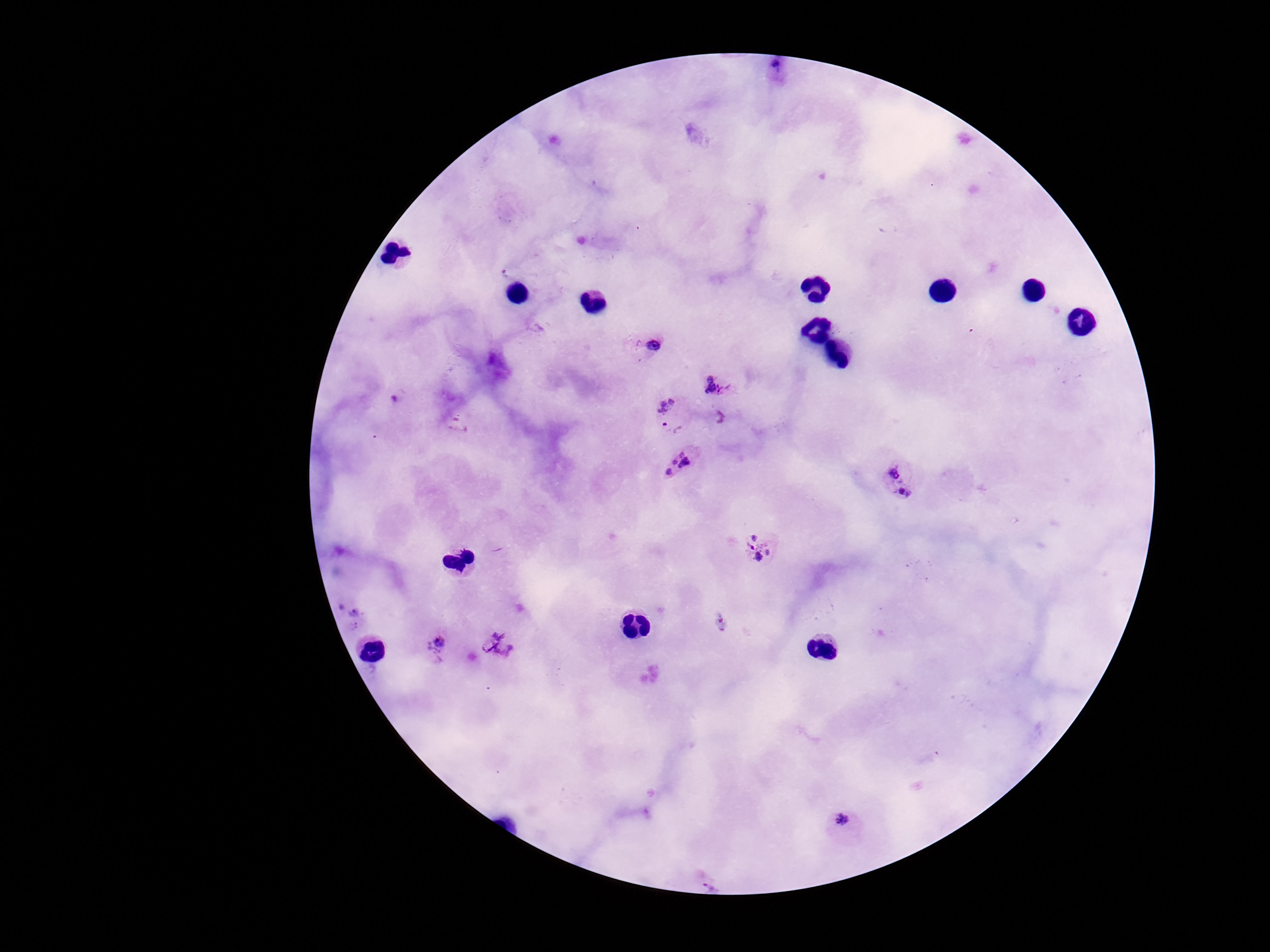

{
  "field_of_view": "single",
  "image_size": "1270×952 pixels",
  "plasmodium_parasite_locations": "approximate object centers, in pixels from the top-left corner: (x=776, y=73), (x=643, y=343), (x=716, y=385), (x=672, y=416), (x=682, y=463), (x=899, y=482), (x=762, y=548), (x=352, y=615), (x=436, y=646), (x=498, y=647), (x=844, y=827), (x=711, y=882)",
  "patient_malaria_status": "positive",
  "capture": "smartphone camera through the microscope eyepiece",
  "preparation": "thick blood smear",
  "magnification": "100x",
  "stain": "Giemsa"
}